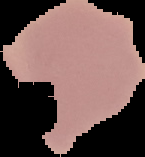
image type = segmented cell region with the area outside set to black
malaria status = uninfected
image size = 145×157 pixels
preparation = thin blood film